Locate platelets.
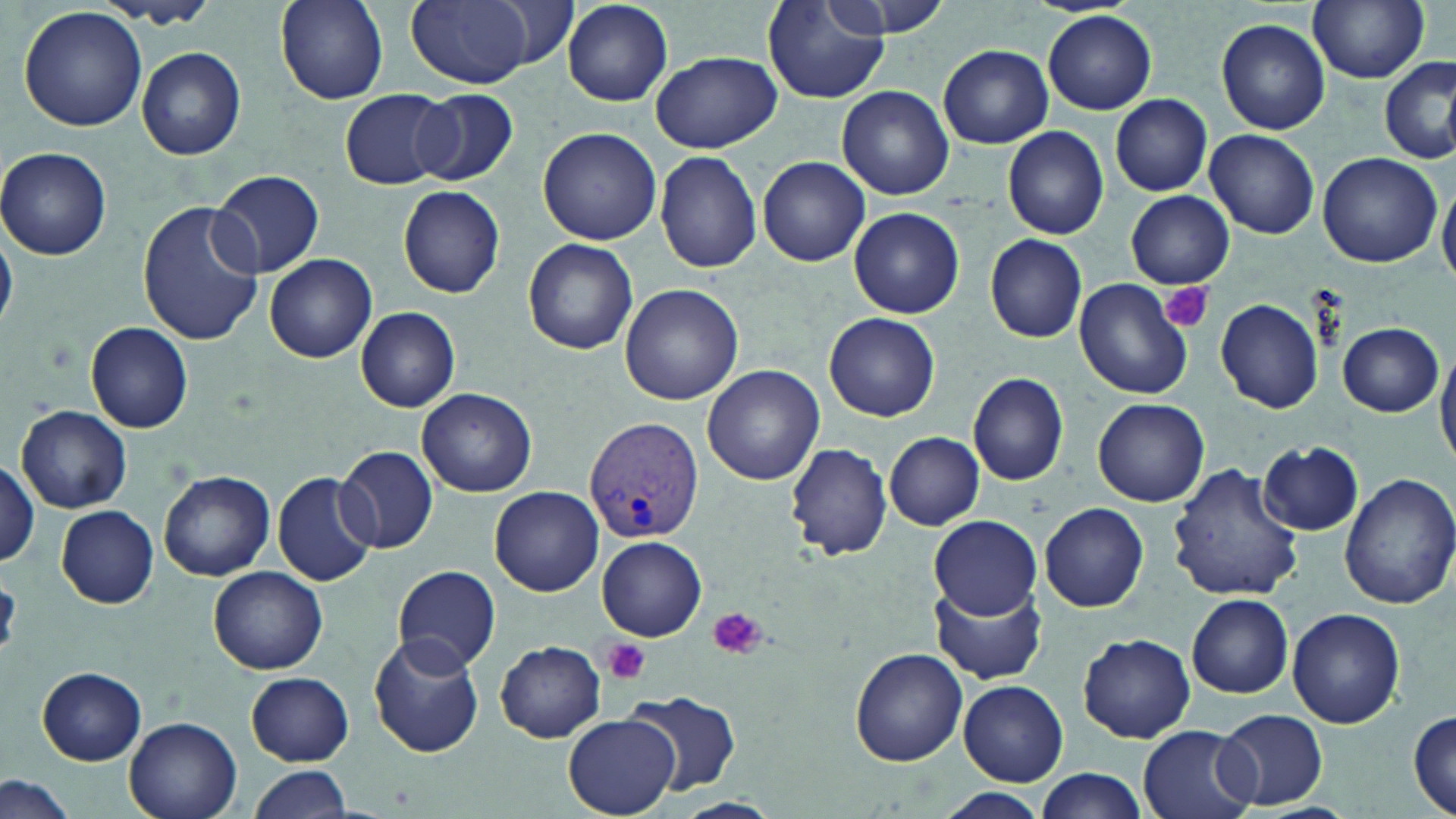

Approximate bounding boxes as named x1/y1/x2/y2 corners in pixels.
Platelets: (x1=1161, y1=282, x2=1213, y2=333), (x1=708, y1=607, x2=766, y2=661), (x1=601, y1=638, x2=652, y2=684).

slide_level_diagnosis: Plasmodium vivax
uninfected_red_blood_cell_locations: 'approximate bounding boxes as named x1/y1/x2/y2 corners in pixels: (x1=273, y1=0, x2=390, y2=107), (x1=406, y1=0, x2=538, y2=87), (x1=820, y1=0, x2=956, y2=41), (x1=1027, y1=0, x2=1141, y2=17), (x1=96, y1=1, x2=220, y2=29), (x1=1308, y1=1, x2=1428, y2=85), (x1=562, y1=2, x2=674, y2=106), (x1=761, y1=3, x2=887, y2=105), (x1=18, y1=6, x2=149, y2=134), (x1=1043, y1=9, x2=1156, y2=115), (x1=1216, y1=17, x2=1330, y2=133), (x1=939, y1=44, x2=1053, y2=149), (x1=136, y1=47, x2=245, y2=161), (x1=652, y1=51, x2=781, y2=153), (x1=1379, y1=57, x2=1455, y2=164), (x1=837, y1=85, x2=954, y2=200), (x1=340, y1=89, x2=453, y2=189), (x1=411, y1=89, x2=517, y2=185), (x1=1110, y1=94, x2=1212, y2=197), (x1=537, y1=126, x2=662, y2=244), (x1=1001, y1=127, x2=1110, y2=239), (x1=1205, y1=129, x2=1319, y2=238), (x1=0, y1=145, x2=113, y2=259), (x1=655, y1=151, x2=762, y2=274), (x1=1317, y1=151, x2=1443, y2=267), (x1=758, y1=157, x2=870, y2=267), (x1=211, y1=170, x2=325, y2=278), (x1=1438, y1=183, x2=1456, y2=288), (x1=397, y1=184, x2=505, y2=298), (x1=1125, y1=191, x2=1234, y2=288), (x1=137, y1=201, x2=265, y2=347), (x1=847, y1=208, x2=963, y2=316), (x1=0, y1=228, x2=19, y2=333), (x1=983, y1=233, x2=1087, y2=342), (x1=523, y1=237, x2=638, y2=354), (x1=265, y1=253, x2=378, y2=363), (x1=1074, y1=276, x2=1196, y2=400), (x1=621, y1=284, x2=741, y2=405), (x1=1216, y1=299, x2=1322, y2=412), (x1=356, y1=307, x2=460, y2=412), (x1=824, y1=313, x2=939, y2=422), (x1=86, y1=322, x2=192, y2=433), (x1=1336, y1=323, x2=1444, y2=417), (x1=1436, y1=341, x2=1456, y2=467), (x1=703, y1=364, x2=825, y2=484), (x1=969, y1=372, x2=1070, y2=486), (x1=416, y1=388, x2=537, y2=497), (x1=1094, y1=397, x2=1209, y2=507), (x1=18, y1=405, x2=133, y2=513), (x1=884, y1=431, x2=986, y2=529), (x1=787, y1=442, x2=893, y2=561), (x1=1260, y1=442, x2=1364, y2=536), (x1=336, y1=445, x2=439, y2=553), (x1=0, y1=459, x2=40, y2=566), (x1=1168, y1=459, x2=1303, y2=602), (x1=157, y1=469, x2=275, y2=582), (x1=272, y1=470, x2=379, y2=587), (x1=1340, y1=472, x2=1454, y2=609), (x1=491, y1=486, x2=603, y2=596), (x1=1040, y1=502, x2=1149, y2=612), (x1=56, y1=504, x2=158, y2=606), (x1=928, y1=515, x2=1043, y2=620), (x1=597, y1=537, x2=707, y2=640), (x1=208, y1=565, x2=328, y2=674), (x1=393, y1=565, x2=501, y2=672), (x1=932, y1=584, x2=1048, y2=684), (x1=947, y1=586, x2=1058, y2=784), (x1=1188, y1=594, x2=1293, y2=698), (x1=1286, y1=606, x2=1405, y2=728), (x1=365, y1=631, x2=485, y2=759), (x1=1078, y1=633, x2=1196, y2=742), (x1=496, y1=641, x2=606, y2=742), (x1=848, y1=647, x2=967, y2=766), (x1=36, y1=666, x2=148, y2=764), (x1=244, y1=672, x2=354, y2=764), (x1=958, y1=681, x2=1068, y2=785), (x1=625, y1=692, x2=741, y2=795), (x1=1408, y1=708, x2=1456, y2=816), (x1=1215, y1=709, x2=1328, y2=810), (x1=562, y1=715, x2=681, y2=819), (x1=124, y1=717, x2=241, y2=819), (x1=1137, y1=725, x2=1257, y2=819), (x1=248, y1=764, x2=355, y2=818), (x1=1032, y1=768, x2=1151, y2=819), (x1=0, y1=773, x2=79, y2=819), (x1=937, y1=790, x2=1048, y2=819), (x1=671, y1=797, x2=781, y2=819)'
plasmodium_vivax_infected_red_blood_cell_locations: 'approximate bounding boxes as named x1/y1/x2/y2 corners in pixels: (x1=585, y1=417, x2=705, y2=543)'
preparation: thin blood film
image_size: 1456×819 pixels
stain: May-Grünwald-Giemsa
field_of_view: single
modality: optical microscopy
magnification: 1000x